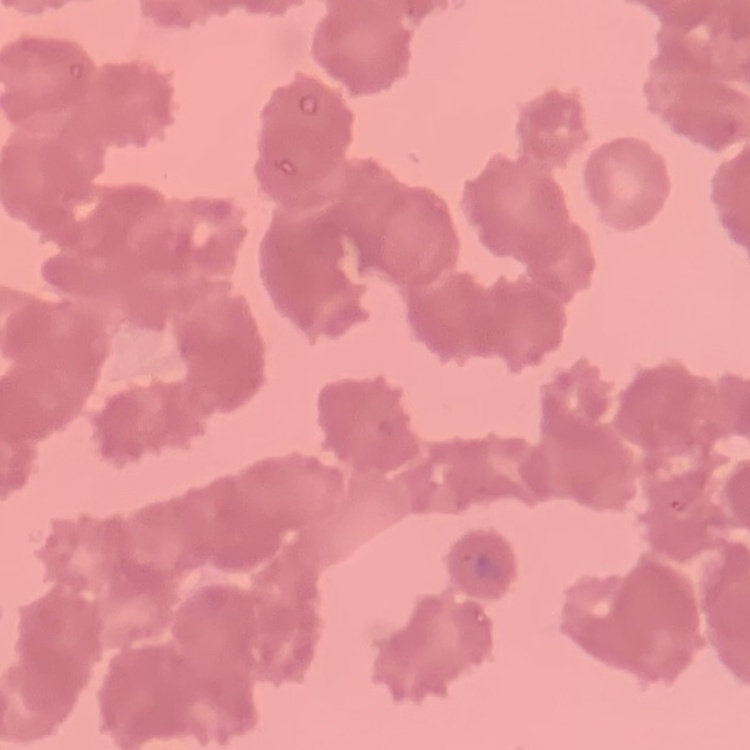
Summary:
  - Erythrocyte morphology: rouleaux formation
  - Stain: Field's or Giemsa
  - Preparation: thin peripheral smear
  - Image type: square crop of a larger photomicrograph